State the preparation type.
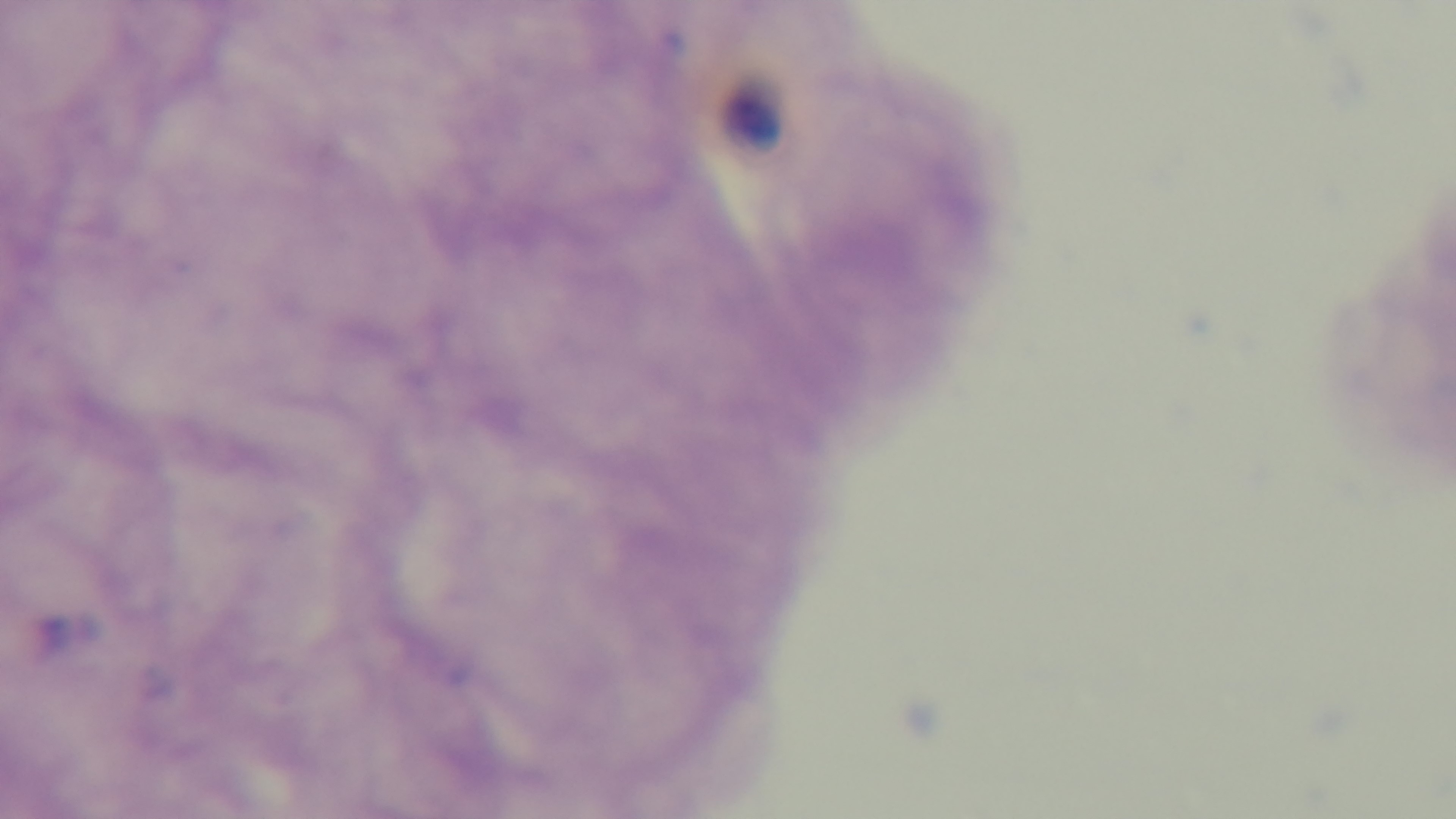
A thick smear.

field_of_view: one from the slide
modality: light microscopy
objective: 100x oil immersion
stain: Giemsa
malaria_status: negative
capture: mounted 4K digital camera